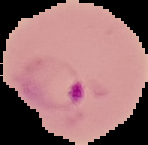 The area outside the segmented cell region is set to black. Result: Plasmodium parasites detected. From a thin blood film. Image is 148×145 pixels.